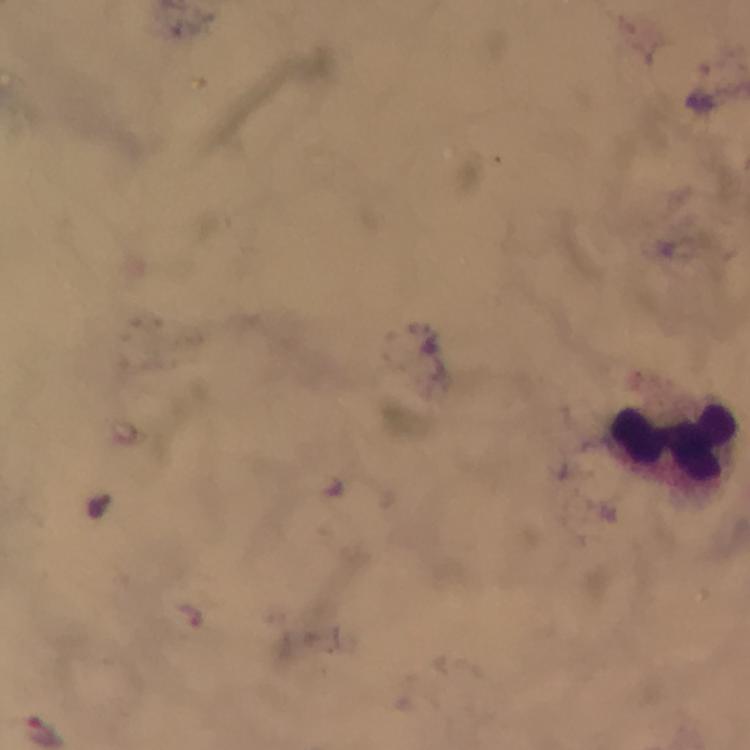

Approximate object centers, in pixels from the top-left corner.
Summary:
  - Leukocyte locations: (x=676, y=445)
  - Plasmodium parasite locations: (x=46, y=731)
  - Preparation: thick blood film
  - Capture: smartphone photograph through a microscope
  - Immersion oil: applied
  - Stain: Giemsa
  - Image size: 750×750 pixels
  - Context: from a malaria diagnostic workup
  - Cropped from: one field of view
  - Magnification: 100x